Assess this cell for malaria.
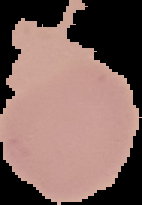
Uninfected.

Summary:
  - Preparation: thin blood smear
  - Image size: 142×205 pixels
  - Image type: cell region segmented out of the field of view; surrounding area masked to black